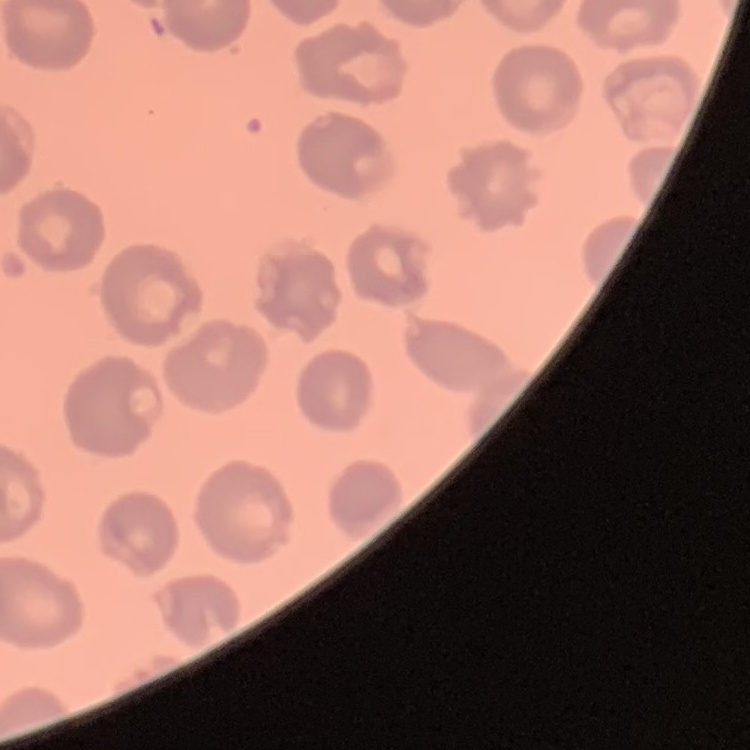
{
  "erythrocyte_morphology": "no rouleaux formation",
  "stain": "Field's or Giemsa",
  "image_type": "square crop of a larger photomicrograph",
  "preparation": "thin blood smear"
}